Identify the parasite.
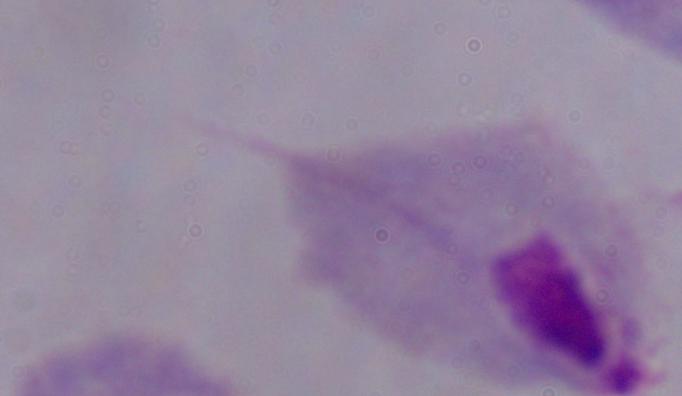

A trichomonad.

magnification = 1000x
modality = photomicrograph